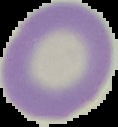
preparation = thin blood film
result = negative for Plasmodium parasites
image size = 118×127 pixels
image type = segmented cell region with the area outside set to black